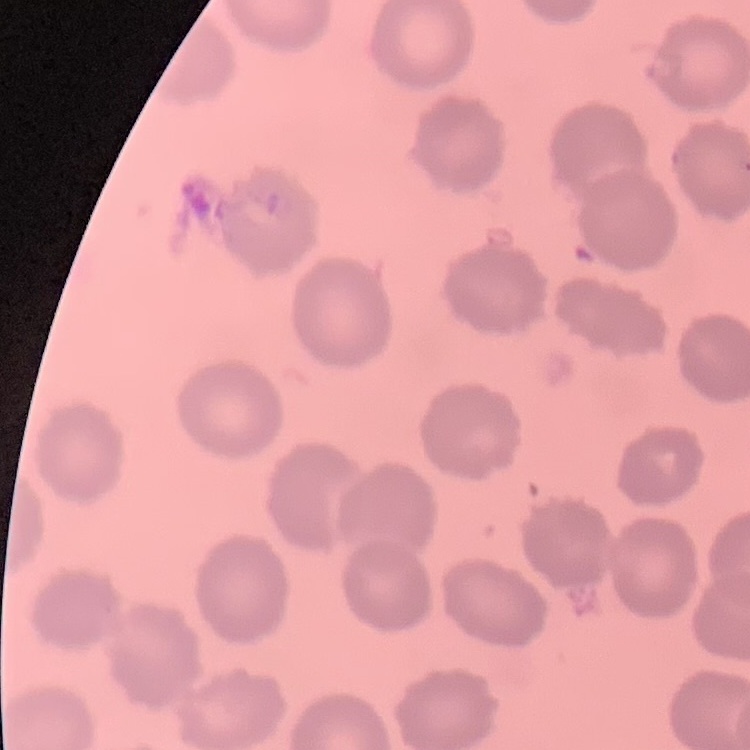

Summary:
  - Red blood cell morphology: no rouleaux formation
  - Preparation: thin peripheral smear
  - Image type: one tile cut from a larger photomicrograph
  - Stain: Field's or Giemsa